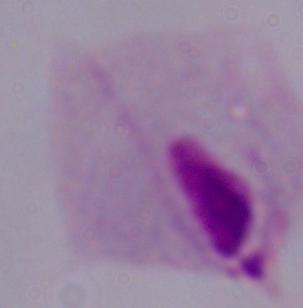
A trichomonad is shown. 1000x magnification. Micrograph.